Identify the preparation type.
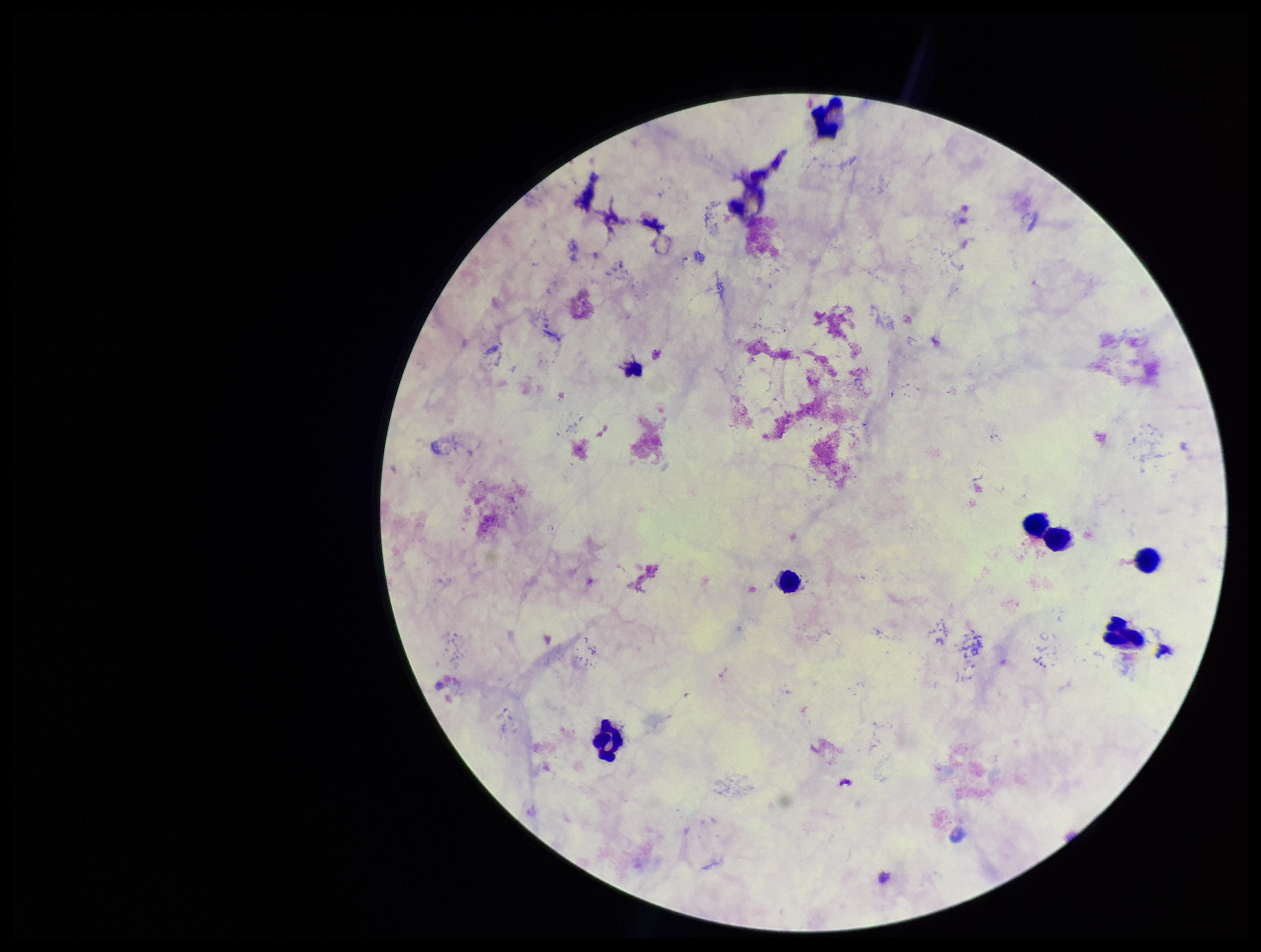

Thick.

{
  "stain": "Giemsa",
  "plasmodium_parasites": "none identified",
  "image_size": "1261×952 pixels",
  "capture": "smartphone photograph through the microscope eyepiece",
  "parasite_count": 0,
  "patient_malaria_status": "negative",
  "leukocyte_count": 6,
  "field_of_view": "one from this slide"
}